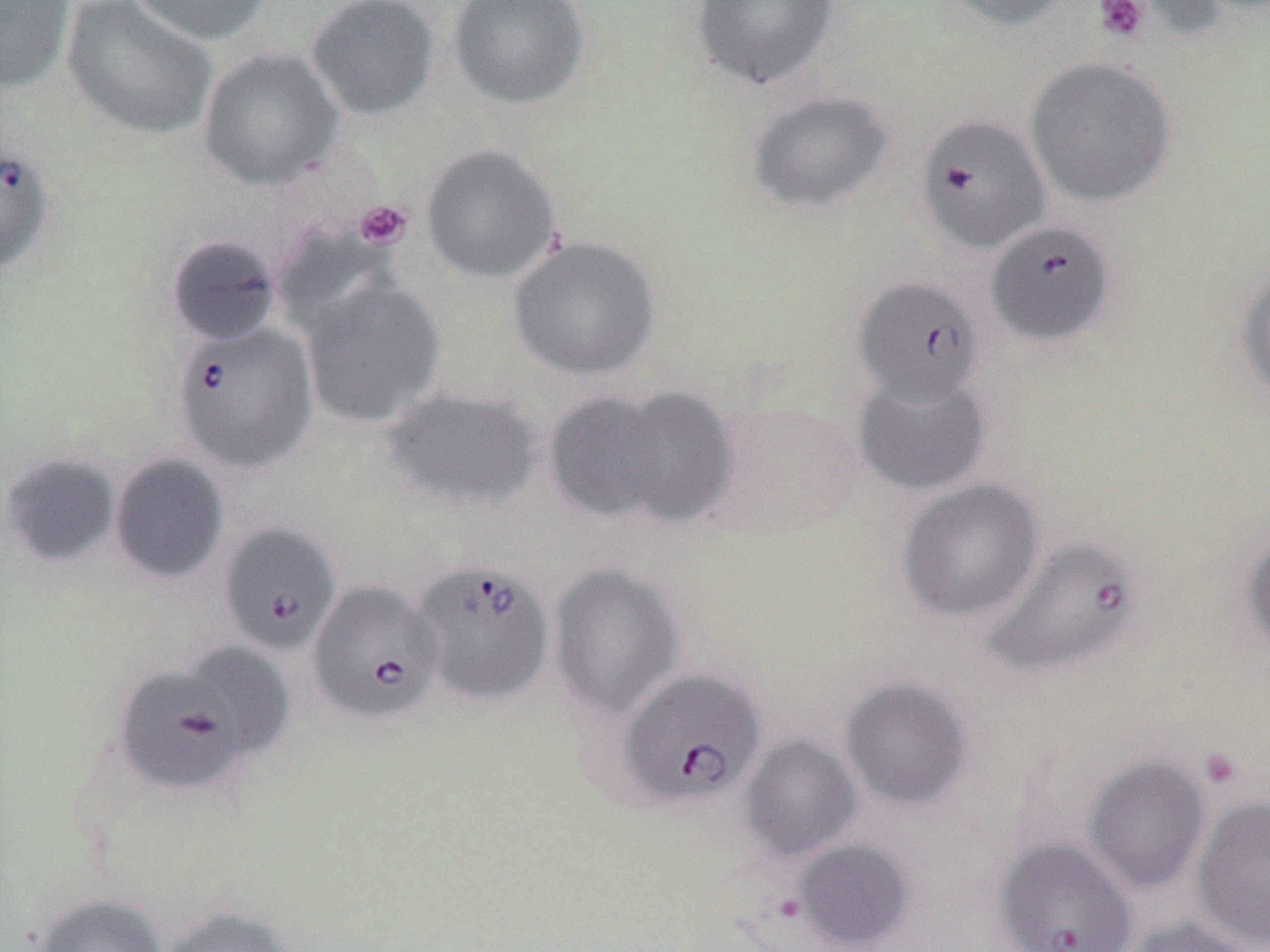
Approximate bounding boxes as (x1,y1)-(x2,y2) corner pairs in pixels. Babesia divergens-infected red blood cell locations: (0,141)-(59,277), (987,219)-(1117,346), (853,276)-(985,404), (171,323)-(318,472), (219,522)-(342,656), (983,534)-(1144,680), (409,557)-(555,707), (307,580)-(444,725), (614,667)-(768,809), (994,838)-(1137,952). Uninfected red blood cell locations: (0,0)-(76,94), (60,0)-(218,141), (128,0)-(274,46), (305,0)-(441,120), (448,0)-(590,110), (942,0)-(1078,32), (690,1)-(841,92), (198,47)-(343,191), (1026,56)-(1177,207), (745,90)-(895,214), (916,113)-(1050,253), (421,144)-(562,284), (271,221)-(402,340), (165,233)-(283,347), (508,235)-(661,381), (1235,263)-(1270,405), (300,278)-(445,428), (852,368)-(992,496), (542,384)-(733,531), (381,386)-(542,514), (700,401)-(863,543), (1,451)-(121,568), (109,452)-(229,585), (896,478)-(1045,623), (1238,524)-(1270,662), (548,561)-(684,721), (110,651)-(277,797), (840,676)-(975,811), (739,735)-(862,861), (1084,756)-(1210,893), (1192,795)-(1270,950), (794,838)-(915,951), (33,893)-(169,952), (157,905)-(300,952), (1124,915)-(1258,952). Platelet locations: (1093,0)-(1149,44), (354,199)-(413,250), (1198,747)-(1245,791). Slide-level diagnosis: Babesia divergens. May-Grünwald-Giemsa stain. Thin blood film. One field of a larger specimen. Captured at 1000x magnification. Light microscopy. Image is 1270×952 pixels.